Classify this cell by malaria status.
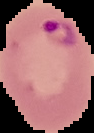
It is parasitized.

preparation = thin blood film
image type = segmented cell region on a black background
image size = 94×133 pixels